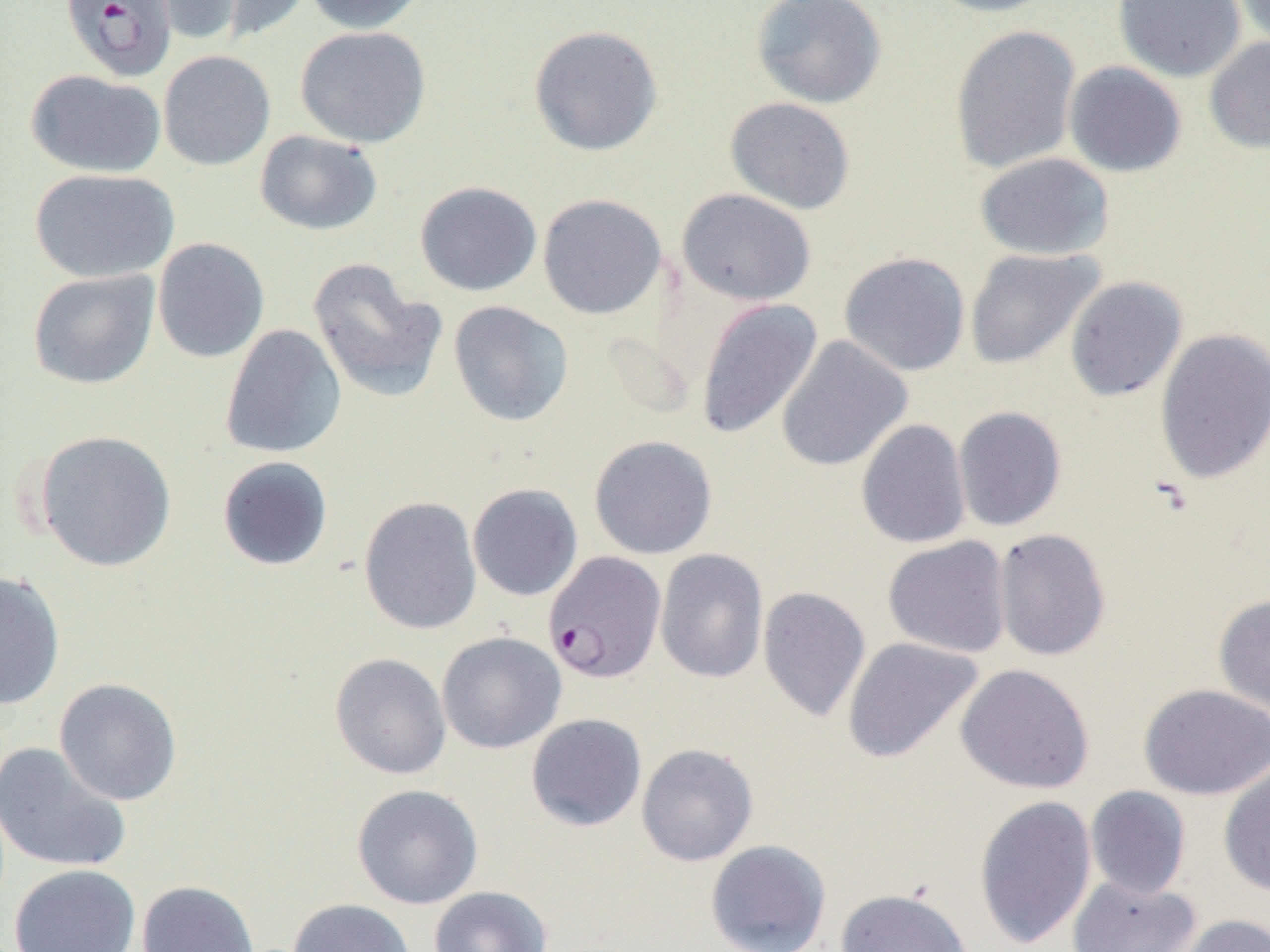

slide-level diagnosis = Plasmodium falciparum
magnification = 1000x
field of view = single
uninfected red blood cell locations = approximate bounding boxes as named x1/y1/x2/y2 corners in pixels: (x1=145, y1=0, x2=243, y2=44), (x1=212, y1=0, x2=312, y2=42), (x1=302, y1=0, x2=426, y2=34), (x1=751, y1=0, x2=887, y2=109), (x1=922, y1=0, x2=1060, y2=17), (x1=1113, y1=0, x2=1245, y2=82), (x1=1233, y1=0, x2=1270, y2=51), (x1=528, y1=24, x2=663, y2=157), (x1=950, y1=24, x2=1081, y2=174), (x1=294, y1=25, x2=431, y2=148), (x1=1204, y1=36, x2=1270, y2=154), (x1=158, y1=50, x2=276, y2=171), (x1=1064, y1=62, x2=1187, y2=178), (x1=26, y1=69, x2=166, y2=178), (x1=725, y1=97, x2=856, y2=215), (x1=255, y1=129, x2=383, y2=235), (x1=975, y1=151, x2=1114, y2=260), (x1=29, y1=168, x2=179, y2=283), (x1=414, y1=180, x2=542, y2=296), (x1=677, y1=188, x2=816, y2=306), (x1=537, y1=193, x2=667, y2=319), (x1=152, y1=237, x2=270, y2=363), (x1=965, y1=247, x2=1103, y2=369), (x1=839, y1=252, x2=970, y2=376), (x1=308, y1=258, x2=447, y2=403), (x1=27, y1=269, x2=160, y2=389), (x1=1065, y1=276, x2=1187, y2=401), (x1=695, y1=298, x2=823, y2=440), (x1=448, y1=301, x2=574, y2=427), (x1=219, y1=323, x2=347, y2=459), (x1=1155, y1=327, x2=1270, y2=484), (x1=776, y1=335, x2=912, y2=472), (x1=953, y1=406, x2=1067, y2=532), (x1=856, y1=418, x2=971, y2=549), (x1=33, y1=429, x2=177, y2=572), (x1=589, y1=434, x2=718, y2=559), (x1=217, y1=456, x2=334, y2=571), (x1=467, y1=483, x2=583, y2=601), (x1=359, y1=496, x2=482, y2=635), (x1=993, y1=528, x2=1110, y2=661), (x1=883, y1=536, x2=1012, y2=658), (x1=655, y1=548, x2=768, y2=684), (x1=0, y1=570, x2=66, y2=710), (x1=757, y1=586, x2=871, y2=723), (x1=1213, y1=593, x2=1270, y2=717), (x1=436, y1=631, x2=567, y2=754), (x1=842, y1=636, x2=984, y2=764), (x1=330, y1=653, x2=452, y2=780), (x1=955, y1=663, x2=1095, y2=794), (x1=53, y1=678, x2=182, y2=806), (x1=1138, y1=683, x2=1270, y2=800), (x1=526, y1=713, x2=647, y2=832), (x1=0, y1=741, x2=132, y2=874), (x1=636, y1=743, x2=758, y2=866), (x1=1218, y1=761, x2=1270, y2=897), (x1=351, y1=783, x2=484, y2=909), (x1=1085, y1=786, x2=1191, y2=899), (x1=974, y1=794, x2=1097, y2=949), (x1=705, y1=839, x2=831, y2=952), (x1=10, y1=863, x2=141, y2=952), (x1=1068, y1=876, x2=1202, y2=952), (x1=137, y1=880, x2=259, y2=952), (x1=429, y1=886, x2=553, y2=952), (x1=835, y1=887, x2=974, y2=952), (x1=286, y1=898, x2=417, y2=952), (x1=1173, y1=914, x2=1270, y2=952)
image size = 1270×952 pixels
preparation = thin blood film
modality = optical microscopy
Plasmodium falciparum-infected red blood cell locations = approximate bounding boxes as named x1/y1/x2/y2 corners in pixels: (x1=60, y1=0, x2=178, y2=82), (x1=543, y1=550, x2=667, y2=683)